Classify this cell by malaria status.
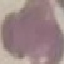
It is uninfected.

Summary:
  - Preparation: thin smear
  - Stain: Giemsa
  - Capture: smartphone through the microscope eyepiece
  - Image type: automatically extracted cell patch, resized to 64 × 64 pixels